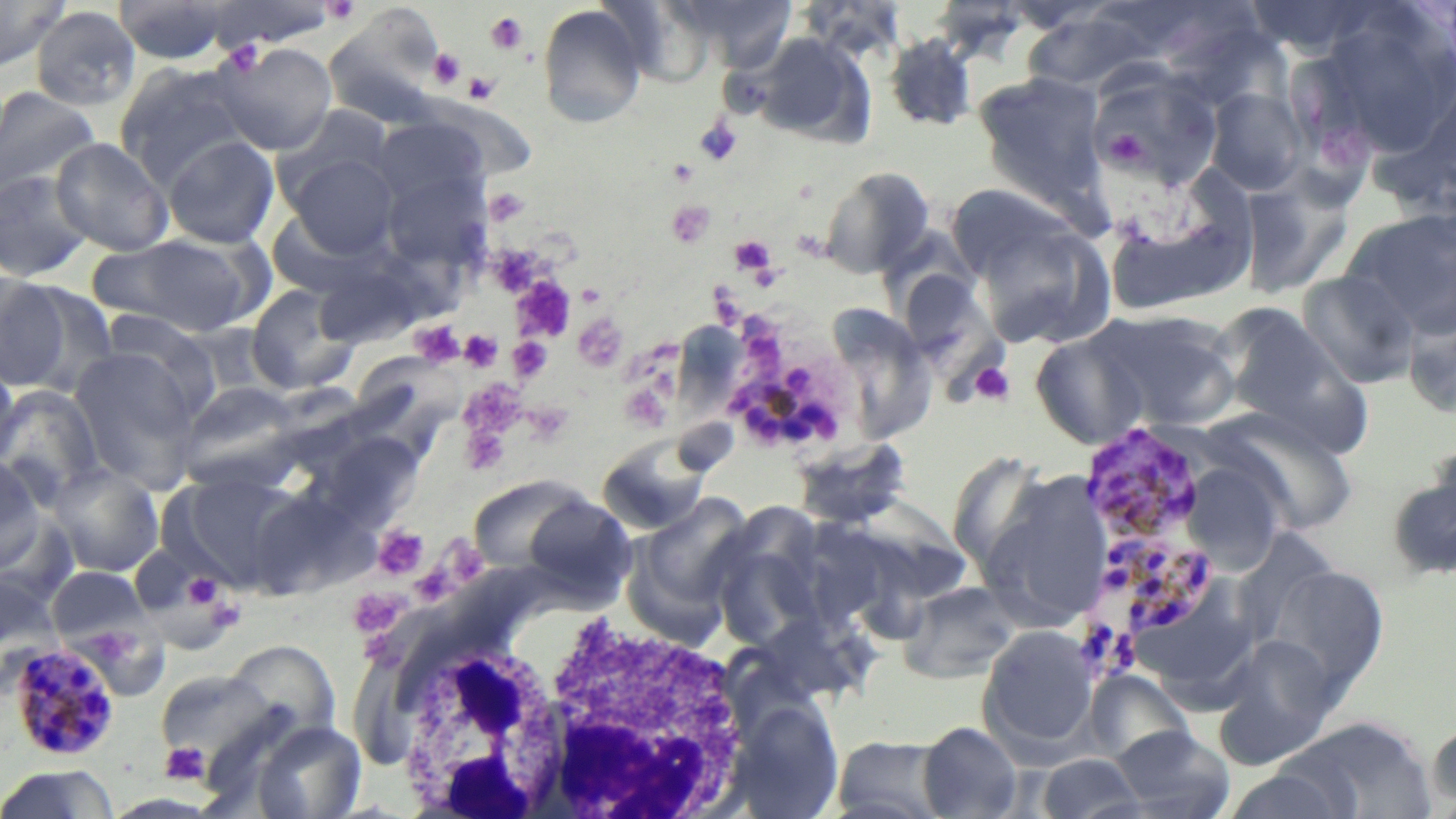

{
  "slide_level_diagnosis": "Plasmodium malariae",
  "preparation": "thin blood film",
  "image_size": "1456×819 pixels",
  "modality": "light microscopy",
  "plasmodium_malariae_infected_red_blood_cell_locations": "approximate bounding boxes as named x1/y1/x2/y2 corners in pixels: (x1=715, y1=316, x2=858, y2=459), (x1=1081, y1=422, x2=1208, y2=551), (x1=1103, y1=539, x2=1217, y2=637), (x1=13, y1=642, x2=128, y2=764)",
  "white_blood_cell_locations": "approximate bounding boxes as named x1/y1/x2/y2 corners in pixels: (x1=397, y1=590, x2=752, y2=817)",
  "platelet_locations": "approximate bounding boxes as named x1/y1/x2/y2 corners in pixels: (x1=322, y1=0, x2=362, y2=24), (x1=485, y1=10, x2=529, y2=55), (x1=220, y1=41, x2=265, y2=75), (x1=428, y1=48, x2=466, y2=90), (x1=463, y1=72, x2=499, y2=104), (x1=694, y1=116, x2=741, y2=165), (x1=668, y1=158, x2=698, y2=186), (x1=485, y1=187, x2=530, y2=226), (x1=667, y1=201, x2=716, y2=248), (x1=731, y1=236, x2=776, y2=275), (x1=495, y1=247, x2=544, y2=297), (x1=512, y1=275, x2=577, y2=343), (x1=708, y1=286, x2=747, y2=329), (x1=573, y1=314, x2=627, y2=373), (x1=411, y1=321, x2=465, y2=368), (x1=460, y1=329, x2=504, y2=372), (x1=509, y1=337, x2=554, y2=383), (x1=970, y1=362, x2=1015, y2=406), (x1=460, y1=379, x2=526, y2=439), (x1=623, y1=388, x2=670, y2=436), (x1=521, y1=402, x2=573, y2=445), (x1=461, y1=423, x2=510, y2=476), (x1=373, y1=526, x2=429, y2=578), (x1=182, y1=571, x2=225, y2=612), (x1=349, y1=588, x2=402, y2=638), (x1=204, y1=596, x2=246, y2=633), (x1=160, y1=742, x2=211, y2=786)",
  "stain": "May-Grünwald-Giemsa",
  "uninfected_red_blood_cell_locations": "approximate bounding boxes as named x1/y1/x2/y2 corners in pixels: (x1=0, y1=0, x2=70, y2=71), (x1=598, y1=0, x2=713, y2=88), (x1=675, y1=0, x2=799, y2=71), (x1=800, y1=0, x2=907, y2=63), (x1=113, y1=1, x2=232, y2=64), (x1=199, y1=1, x2=342, y2=51), (x1=931, y1=2, x2=1029, y2=65), (x1=537, y1=4, x2=648, y2=128), (x1=30, y1=5, x2=142, y2=112), (x1=1022, y1=11, x2=1156, y2=95), (x1=1310, y1=13, x2=1456, y2=165), (x1=1173, y1=29, x2=1300, y2=113), (x1=751, y1=33, x2=873, y2=147), (x1=884, y1=35, x2=978, y2=132), (x1=212, y1=41, x2=337, y2=155), (x1=114, y1=62, x2=256, y2=188), (x1=1087, y1=64, x2=1223, y2=193), (x1=974, y1=74, x2=1109, y2=211), (x1=0, y1=86, x2=101, y2=199), (x1=1205, y1=88, x2=1308, y2=195), (x1=276, y1=105, x2=395, y2=202), (x1=370, y1=117, x2=488, y2=213), (x1=161, y1=135, x2=280, y2=249), (x1=50, y1=137, x2=174, y2=256), (x1=284, y1=152, x2=399, y2=258), (x1=818, y1=166, x2=935, y2=279), (x1=0, y1=169, x2=95, y2=283), (x1=381, y1=170, x2=491, y2=274), (x1=1238, y1=174, x2=1355, y2=299), (x1=1111, y1=175, x2=1252, y2=316), (x1=960, y1=200, x2=1116, y2=350), (x1=267, y1=208, x2=374, y2=298), (x1=1343, y1=209, x2=1456, y2=340), (x1=89, y1=232, x2=264, y2=337), (x1=315, y1=267, x2=460, y2=348), (x1=1298, y1=272, x2=1419, y2=389), (x1=906, y1=273, x2=1008, y2=407), (x1=0, y1=275, x2=72, y2=391), (x1=13, y1=282, x2=119, y2=398), (x1=246, y1=283, x2=359, y2=395), (x1=1214, y1=301, x2=1366, y2=449), (x1=835, y1=307, x2=941, y2=438), (x1=1092, y1=309, x2=1240, y2=433), (x1=98, y1=310, x2=220, y2=416), (x1=178, y1=322, x2=279, y2=405), (x1=1029, y1=328, x2=1151, y2=449), (x1=69, y1=348, x2=205, y2=492), (x1=0, y1=355, x2=22, y2=472), (x1=177, y1=380, x2=304, y2=486), (x1=0, y1=387, x2=105, y2=506), (x1=1213, y1=412, x2=1359, y2=548), (x1=317, y1=432, x2=424, y2=528), (x1=791, y1=438, x2=912, y2=531), (x1=596, y1=439, x2=713, y2=536), (x1=0, y1=455, x2=46, y2=574), (x1=1180, y1=461, x2=1284, y2=573), (x1=49, y1=462, x2=165, y2=577), (x1=1386, y1=465, x2=1456, y2=582), (x1=978, y1=469, x2=1113, y2=631), (x1=170, y1=470, x2=308, y2=591), (x1=467, y1=474, x2=597, y2=576), (x1=628, y1=494, x2=757, y2=631), (x1=517, y1=495, x2=637, y2=601), (x1=709, y1=525, x2=826, y2=651), (x1=846, y1=526, x2=928, y2=648), (x1=1267, y1=564, x2=1389, y2=694), (x1=48, y1=566, x2=152, y2=650), (x1=0, y1=575, x2=65, y2=698), (x1=898, y1=581, x2=1021, y2=684), (x1=978, y1=625, x2=1101, y2=755), (x1=1215, y1=635, x2=1341, y2=764), (x1=221, y1=639, x2=340, y2=745), (x1=155, y1=668, x2=282, y2=768), (x1=1082, y1=671, x2=1193, y2=765), (x1=726, y1=699, x2=844, y2=818), (x1=1290, y1=716, x2=1436, y2=818), (x1=1426, y1=716, x2=1456, y2=813), (x1=252, y1=720, x2=366, y2=819), (x1=917, y1=721, x2=1023, y2=818), (x1=1112, y1=725, x2=1235, y2=819), (x1=830, y1=735, x2=952, y2=819), (x1=1035, y1=753, x2=1146, y2=818), (x1=0, y1=764, x2=120, y2=819), (x1=1220, y1=767, x2=1356, y2=819)",
  "field_of_view": "single",
  "magnification": "1000x"
}